Identify the parasite.
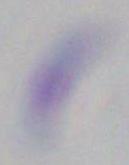
This is Toxoplasma gondii.

Summary:
  - Modality: photomicrograph
  - Magnification: 1000x